Classify this cell by malaria status.
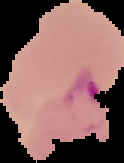

It is uninfected.

Summary:
  - Preparation: thin blood smear
  - Image type: cell region segmented out of the field of view; surrounding area masked to black
  - Image size: 124×163 pixels